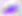

Toxoplasma gondii is seen. Captured at 400x magnification. Photomicrograph.